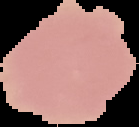
image type = segmented cell region with the area outside set to black
malaria status = uninfected
image size = 139×127 pixels
preparation = thin blood smear